Describe the morphology of the red blood cells.
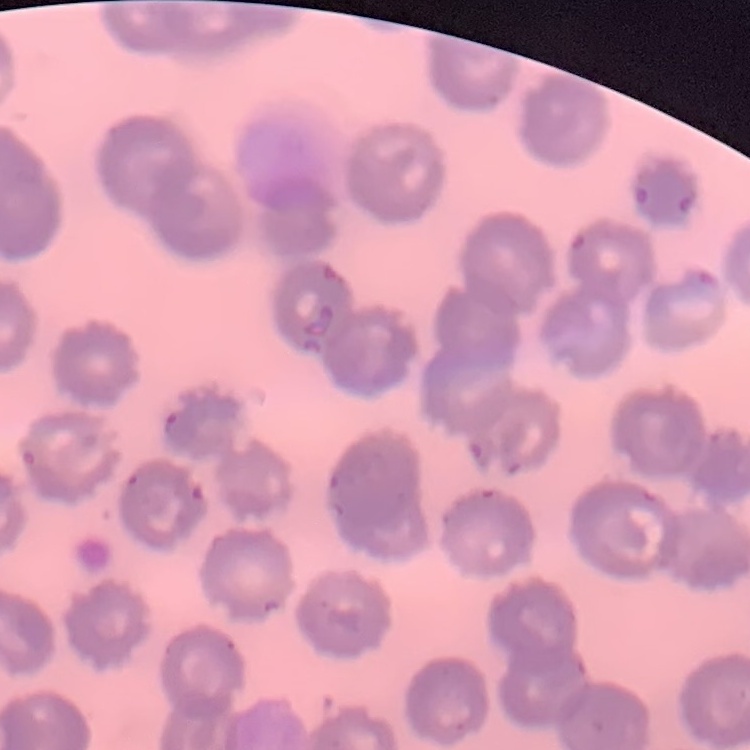

No rouleaux formation.

Thin blood smear. Field's or Giemsa stain. One tile cut from a larger photomicrograph.